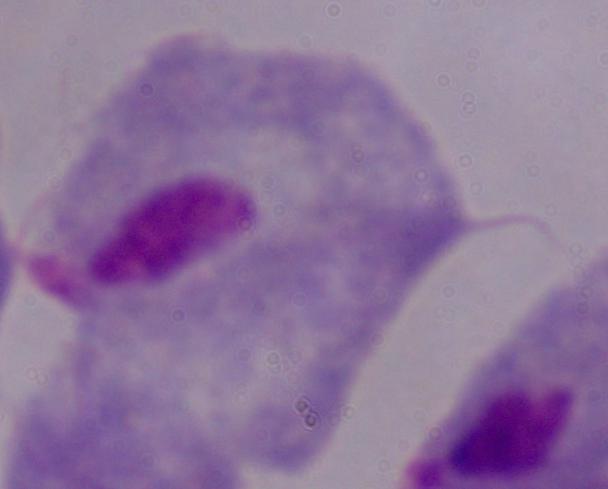

magnification = 1000x
modality = photomicrograph
identification = trichomonad